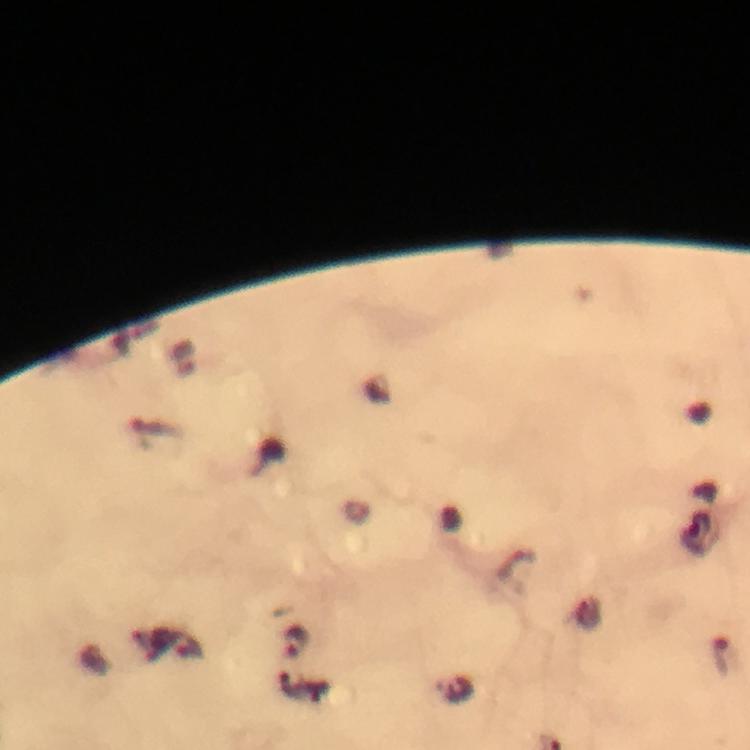

Approximate centers as [x, y] in pixels. Plasmodium parasite locations: [187, 356], [295, 642]. Photographed with a smartphone mounted on the microscope. Thick blood film. Giemsa-stained preparation. From a diagnostic examination for malaria. Image is 750×750 pixels. A crop from one field of view. Immersion oil applied. At 100x magnification.